Classify this cell by malaria status.
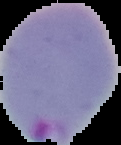

Parasitized.

Image is 121×145 pixels. The area outside the segmented cell region is set to black. From a thin blood smear.